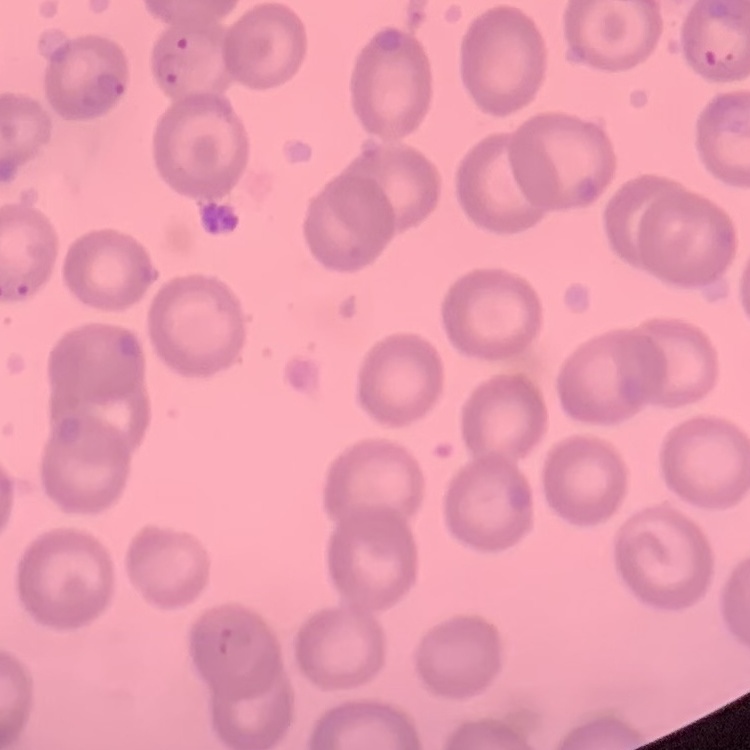
erythrocyte_morphology: no rouleaux formation
stain: Field's or Giemsa
preparation: thin peripheral smear
image_type: one tile cut from a larger photomicrograph